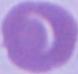
1000x magnification. An erythrocyte is shown. Micrograph.